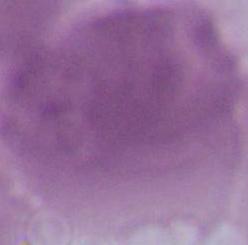

Photomicrograph. A red blood cell is shown. Captured at 1000x magnification.